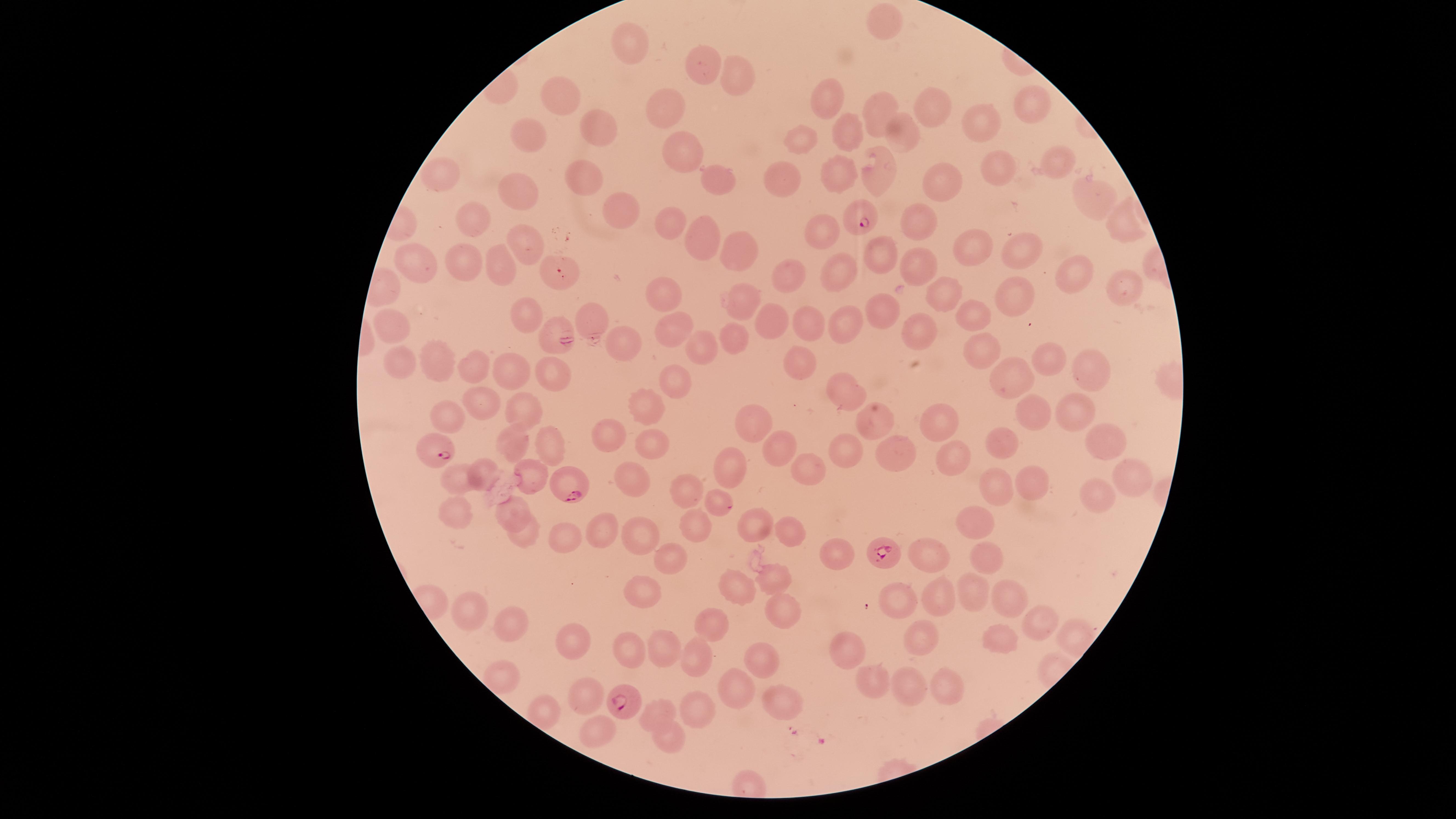 Approximate marker points as (x, y) in pixels. Parasitized red blood cells: (862, 220), (434, 448), (569, 486), (885, 555), (623, 701). Uninfected red blood cells: (887, 28), (632, 44), (704, 63), (741, 81), (563, 95), (838, 95), (875, 105), (1034, 106), (669, 107), (936, 108), (600, 123), (977, 127), (898, 131), (851, 134), (530, 135), (811, 141), (678, 148), (1058, 157), (874, 164), (1003, 166), (584, 172), (839, 173), (446, 176), (783, 177), (714, 178), (937, 184), (1091, 192), (519, 195), (618, 211), (923, 219), (476, 220), (671, 221), (1123, 222), (817, 234), (530, 237), (700, 239), (967, 247), (1014, 249), (740, 251), (877, 252), (920, 262), (424, 264), (465, 265), (840, 267), (1070, 268), (505, 272), (788, 276), (559, 277), (1128, 284), (939, 290), (1023, 291), (668, 295), (742, 302), (884, 304), (521, 308), (973, 311), (593, 316), (775, 318), (806, 318), (385, 319), (855, 322), (917, 327), (674, 328), (553, 329), (730, 337), (702, 344), (624, 346), (978, 347), (1052, 352), (798, 357), (1084, 359), (402, 361), (442, 361), (476, 369), (509, 370), (552, 371), (676, 380), (1015, 380), (842, 383), (476, 397), (647, 406), (518, 407), (1076, 410), (442, 413), (1034, 414), (938, 422), (875, 424), (755, 426), (610, 431), (548, 439), (519, 441), (649, 441), (1107, 441), (1009, 443), (775, 449), (847, 452), (898, 454), (956, 458), (805, 467), (735, 468), (491, 474), (528, 474), (1129, 475), (633, 476), (462, 479), (1027, 480), (996, 488), (685, 490), (719, 494), (1106, 494), (462, 507), (513, 508), (970, 518), (749, 522), (693, 525), (524, 526), (794, 527), (599, 530), (643, 537), (565, 538), (928, 552), (838, 554), (988, 554), (664, 563), (771, 576), (741, 588), (967, 590), (641, 591), (939, 594), (1005, 596), (901, 597), (473, 604), (787, 616), (1039, 622), (716, 625), (514, 626), (1075, 635), (576, 638), (1002, 638), (920, 641), (620, 647), (660, 650), (853, 650), (691, 652), (755, 654), (505, 675), (867, 677), (587, 685), (732, 685), (911, 688), (945, 688), (783, 700), (543, 708), (655, 708), (695, 709), (596, 733), (666, 736). Photographed with a smartphone camera through the microscope eyepiece. One field of view of the specimen. Circular visible region. Giemsa-stained preparation. Thin smear of blood. Presence: malaria parasites identified. Species: Plasmodium falciparum. Image is 1456×819 pixels.